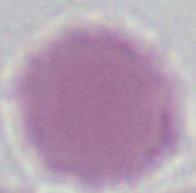

Summary:
  - Magnification: 1000x
  - Identification: red blood cell
  - Modality: micrograph